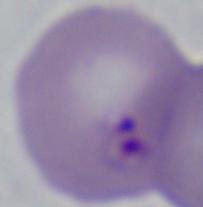
{
  "identification": "Babesia",
  "magnification": "1000x",
  "modality": "photomicrograph"
}